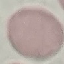
result: no malaria parasites detected
image_type: automatically extracted cell patch, resized to 64 × 64 pixels
stain: Giemsa
capture: smartphone through the microscope eyepiece
preparation: thin smear